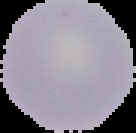
Summary:
  - Image size: 136×133 pixels
  - Preparation: thin blood film
  - Malaria status: uninfected
  - Image type: segmented cell region with the area outside set to black